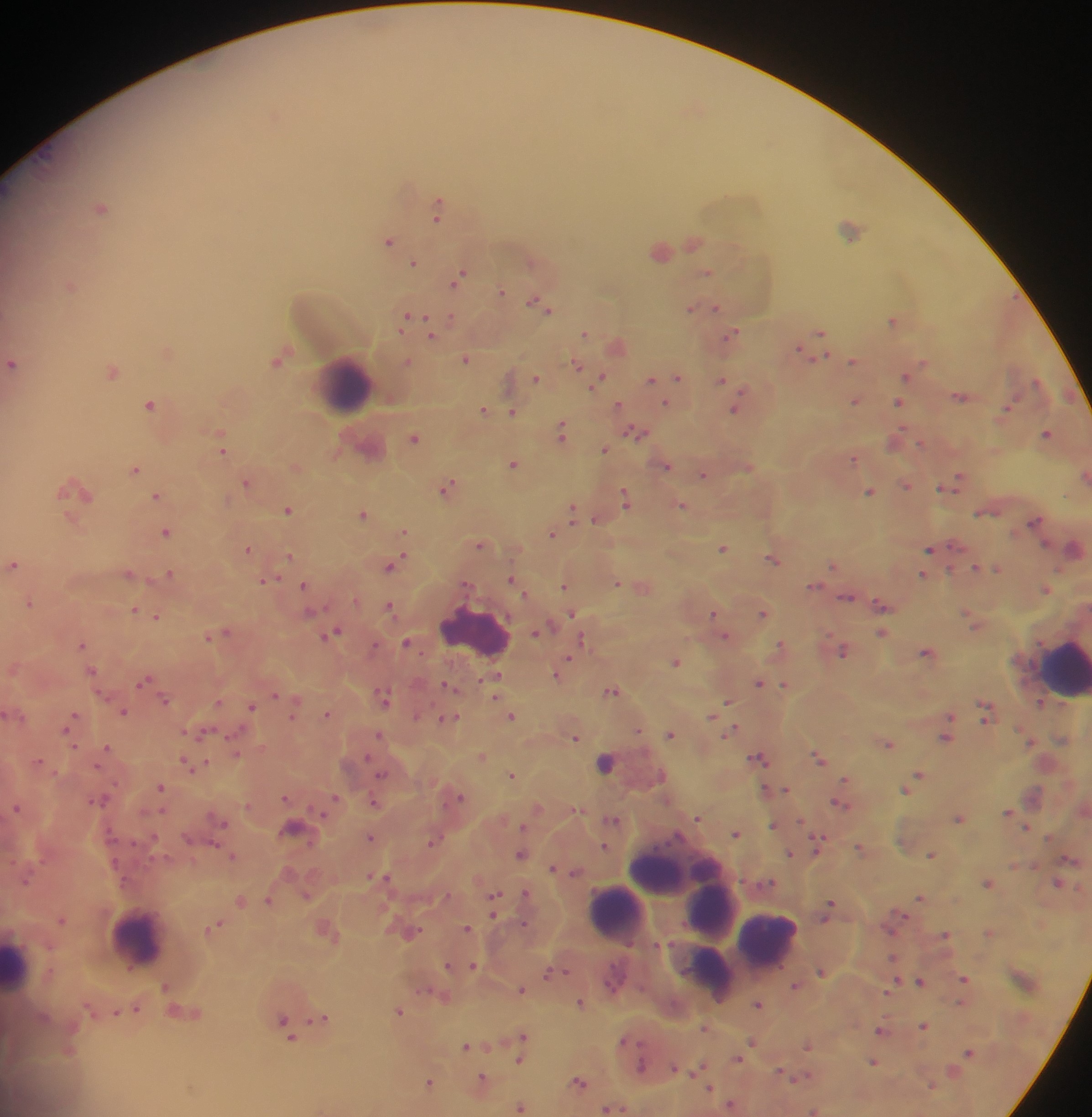
{
  "country": "Ghana",
  "capture": "mobile-phone photograph through a microscope",
  "leukocyte_locations": "approximate centers as x y in pixels: 345 383; 475 632; 1062 669; 678 868; 712 911; 615 912; 138 938; 768 938; 17 964; 711 973",
  "preparation": "thick blood smear",
  "field_of_view": "single",
  "malaria_parasite_locations": "approximate centers as x y in pixels: 697 108; 275 116; 102 207; 439 207; 852 230; 389 240; 693 242; 661 250; 415 263; 706 273; 460 278; 71 285; 501 292; 540 304; 706 306; 693 307; 715 307; 411 318; 452 318; 893 320; 821 331; 585 332; 733 334; 431 335; 618 345; 167 350; 804 351; 467 358; 279 359; 854 361; 407 362; 13 364; 578 366; 113 371; 907 375; 678 377; 537 378; 600 378; 652 379; 722 380; 962 396; 855 400; 900 401; 151 404; 666 404; 619 405; 737 408; 484 410; 1006 410; 513 411; 563 431; 636 432; 1047 433; 414 437; 896 441; 370 445; 222 449; 605 450; 854 458; 514 464; 666 465; 296 466; 749 467; 136 469; 705 474; 1085 476; 248 482; 955 483; 907 485; 449 487; 77 489; 870 491; 157 496; 626 498; 682 505; 573 509; 289 510; 363 513; 596 518; 1036 520; 166 532; 404 532; 553 534; 481 544; 723 547; 1074 548; 249 549; 931 549; 290 555; 773 559; 400 561; 13 564; 392 565; 834 565; 987 566; 996 567; 977 568; 130 573; 170 573; 923 574; 267 579; 514 580; 617 582; 305 585; 642 585; 814 585; 565 586; 1046 588; 848 597; 30 602; 882 604; 390 605; 136 610; 714 613; 764 613; 570 614; 157 616; 973 619; 540 631; 226 632; 883 632; 333 633; 209 636; 725 636; 582 638; 408 643; 83 644; 782 646; 375 647; 844 650; 928 652; 569 660; 675 661; 92 670; 557 673; 495 678; 146 680; 760 682; 785 684; 448 685; 613 691; 275 694; 384 697; 165 700; 728 701; 219 702; 295 702; 1041 704; 252 705; 986 710; 124 711; 11 712; 329 713; 512 715; 713 715; 950 717; 449 718; 71 723; 638 729; 734 730; 201 733; 671 733; 380 735; 947 735; 576 736; 1030 741; 888 743; 107 749; 235 751; 483 756; 759 758; 819 758; 39 761; 605 762; 191 764; 513 774; 920 774; 382 775; 846 778; 913 783; 161 787; 786 789; 907 789; 776 790; 767 791; 286 797; 458 797; 99 799; 334 799; 375 802; 840 803; 17 807; 537 807; 1009 811; 698 818; 959 818; 613 819; 220 820; 802 820; 775 825; 1027 827; 297 828; 737 833; 371 837; 434 841; 819 842; 605 846; 861 847; 790 853; 522 854; 932 854; 233 856; 556 868; 576 872; 382 877; 988 883; 1058 883; 526 893; 307 895; 921 897; 268 899; 495 899; 241 900; 831 905; 494 908; 62 918; 524 924; 215 927; 467 928; 328 930; 410 931; 990 932; 946 935; 894 958; 449 965; 473 965; 552 972; 822 972; 964 978; 921 980; 896 981; 167 986; 796 986; 522 988; 888 991; 442 995; 581 1002; 759 1003; 961 1003; 135 1009; 116 1011; 400 1011; 184 1012; 321 1018; 924 1025; 287 1028; 706 1028; 882 1031; 523 1036; 627 1041; 753 1042; 750 1046; 807 1046; 468 1047; 969 1052; 520 1060; 738 1060; 874 1061; 642 1066; 675 1068; 698 1068; 954 1070; 781 1072; 800 1077; 483 1080; 431 1082; 580 1082; 933 1085; 711 1088; 732 1104; 520 1106; 612 1108; 814 1110",
  "image_size": "1092×1117 pixels"
}